Classify this cell by malaria status.
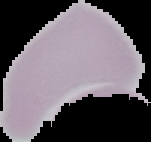

Uninfected.

Summary:
  - Preparation: thin blood smear
  - Image type: segmented cell region with the area outside set to black
  - Image size: 151×142 pixels